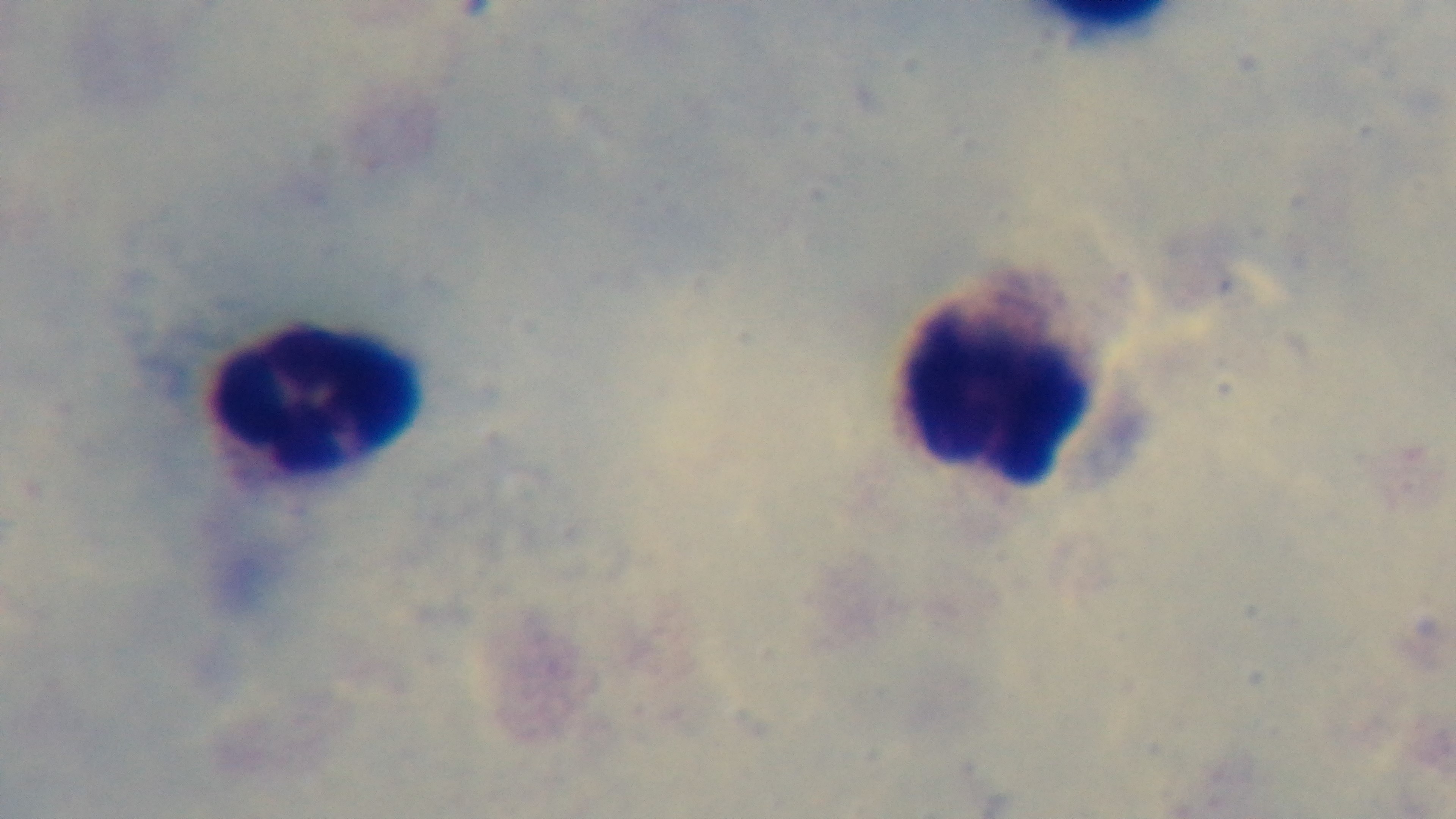
preparation = thick
modality = light microscopy
capture = mounted 4K digital camera
malaria status = uninfected
stain = Giemsa
objective = 100x oil immersion
field of view = single